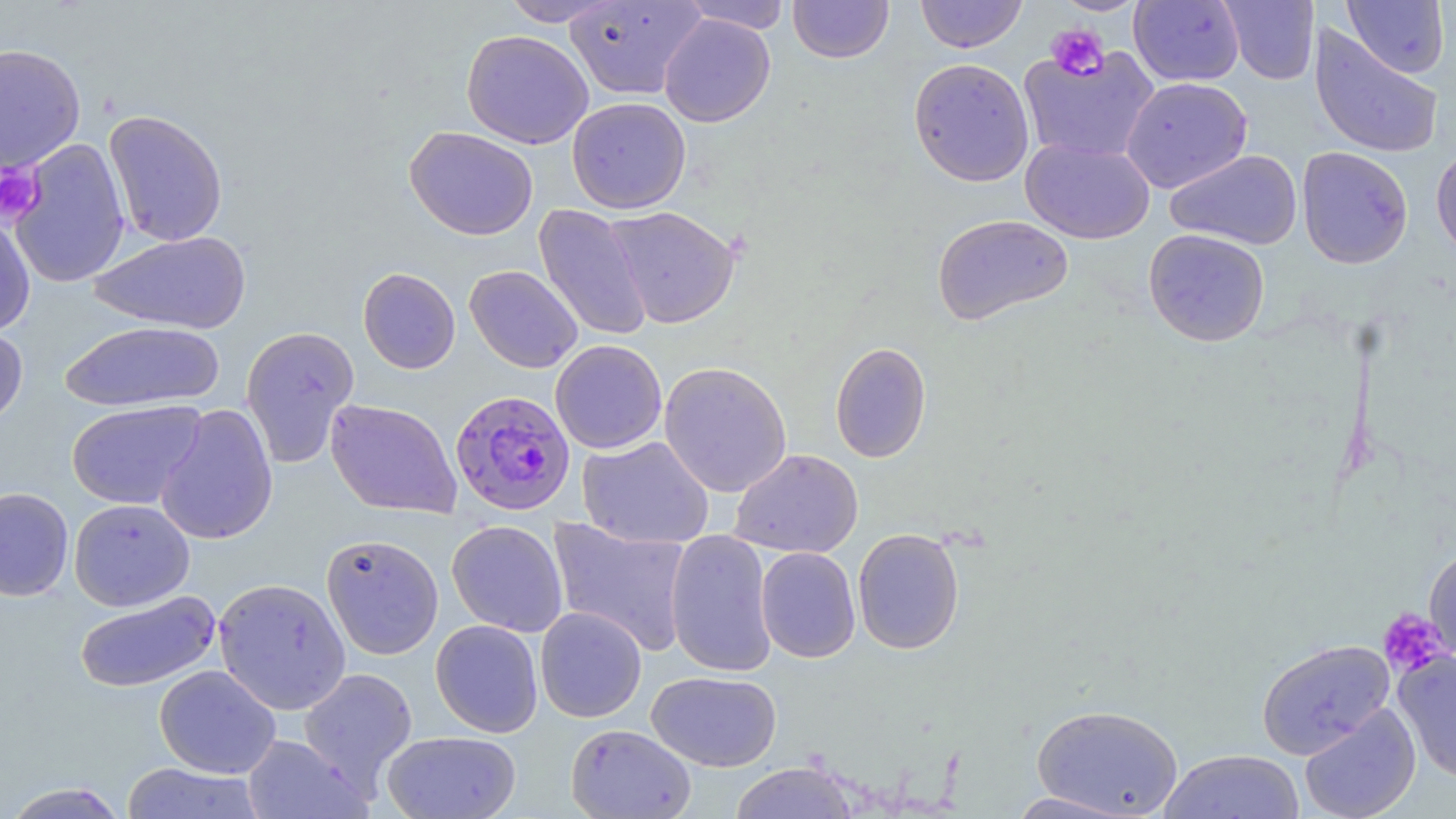
slide-level diagnosis = Plasmodium falciparum
image size = 1456×819 pixels
stain = May-Grünwald-Giemsa
platelet locations = approximate bounding boxes as (x1,y1)-(x2,y2) corner pairs in pixels: (1045,24)-(1110,82), (0,163)-(44,224), (1377,608)-(1451,678)
magnification = 1000x
uninfected red blood cell locations = approximate bounding boxes as (x1,y1)-(x2,y2) corner pairs in pixels: (500,0)-(623,26), (564,0)-(706,101), (788,0)-(894,63), (915,0)-(1027,53), (1051,0)-(1150,15), (1129,0)-(1244,86), (1219,0)-(1319,85), (1342,0)-(1449,78), (680,1)-(792,34), (659,13)-(775,127), (1310,25)-(1443,159), (461,29)-(594,149), (0,43)-(86,174), (1018,45)-(1160,164), (908,57)-(1035,187), (1121,76)-(1252,193), (567,97)-(691,214), (103,109)-(228,247), (404,126)-(538,240), (8,138)-(131,289), (1020,138)-(1154,244), (1431,143)-(1456,261), (1296,146)-(1414,269), (1165,149)-(1303,250), (533,204)-(652,342), (604,205)-(741,329), (0,211)-(36,338), (932,213)-(1073,326), (1143,228)-(1270,347), (89,230)-(252,334), (464,265)-(583,373), (358,267)-(461,374), (60,320)-(224,412), (0,322)-(28,429), (241,325)-(359,468), (550,339)-(667,454), (830,341)-(932,463), (658,361)-(792,498), (325,398)-(462,519), (66,400)-(205,509), (155,403)-(278,546), (577,436)-(714,549), (728,449)-(864,558), (0,487)-(74,601), (68,498)-(195,611), (547,517)-(693,656), (446,519)-(568,637), (852,527)-(965,655), (665,529)-(777,679), (321,533)-(444,660), (1424,542)-(1456,670), (756,547)-(860,663), (213,577)-(351,715), (74,590)-(222,693), (535,606)-(647,722), (430,619)-(544,737), (1256,638)-(1395,759), (1394,650)-(1456,784), (154,665)-(281,778), (298,666)-(419,794), (646,671)-(781,772), (1031,703)-(1183,818), (1299,703)-(1421,819), (566,723)-(696,819), (382,730)-(521,819), (240,734)-(371,819), (1159,749)-(1305,819), (729,761)-(858,818), (120,762)-(266,818), (1,781)-(131,819), (1004,791)-(1140,818)
field of view = single
Plasmodium falciparum-infected red blood cell locations = approximate bounding boxes as (x1,y1)-(x2,y2) corner pairs in pixels: (451,389)-(576,515)
preparation = thin blood smear
modality = light microscopy